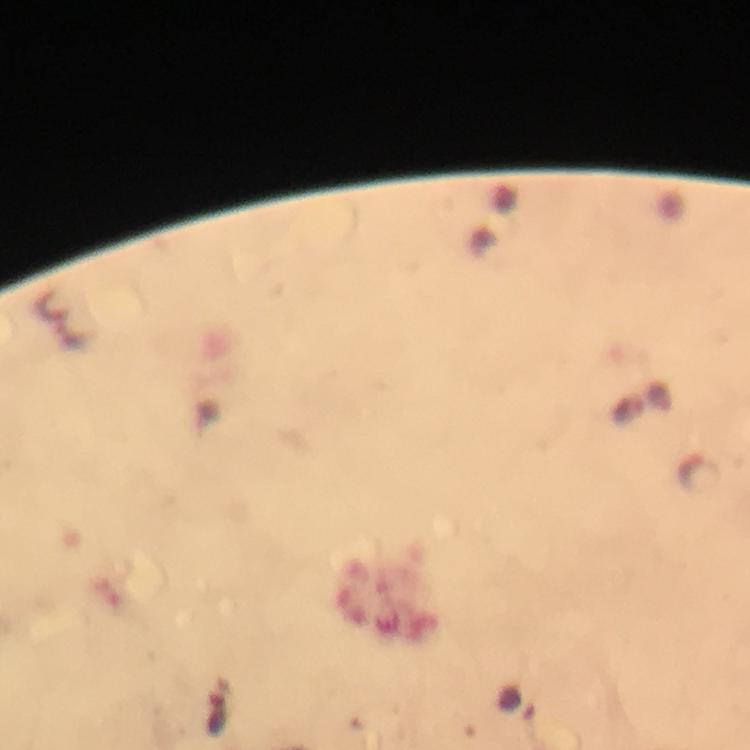
Approximate centers as {x, y} in pixels.
Summary:
  - Plasmodium parasite locations: {627, 413}, {698, 473}
  - Cropped from: a single field of view
  - Capture: smartphone photograph through a microscope
  - Preparation: thick blood film
  - Context: from a diagnostic examination for malaria
  - Immersion oil: used
  - Image size: 750×750 pixels
  - Magnification: 100x
  - Stain: Giemsa